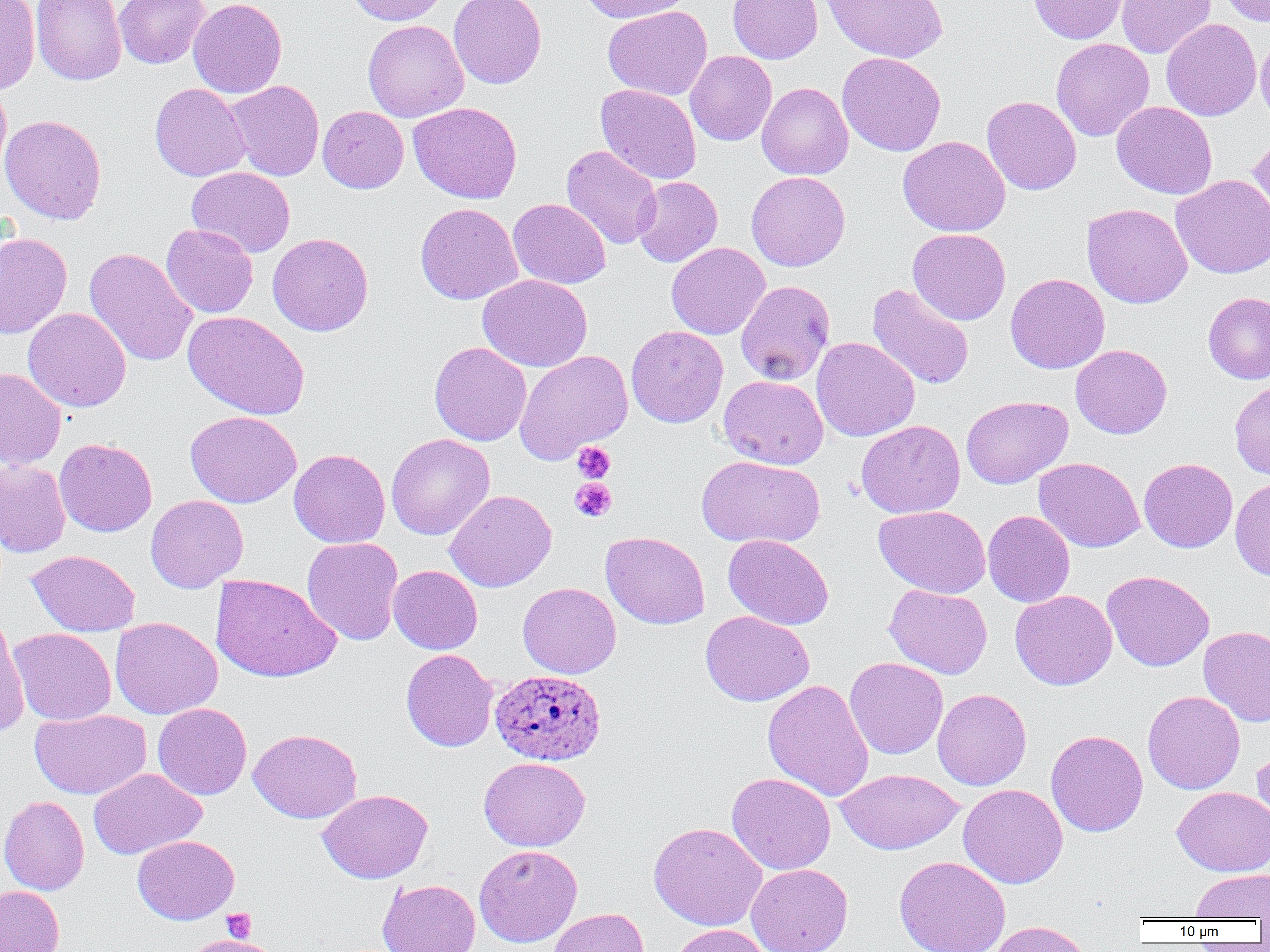
slide-level diagnosis = Plasmodium ovale
magnification = 1000x
image size = 1270×952 pixels
field of view = single
Plasmodium ovale-infected red blood cell locations = approximate bounding boxes as named x1/y1/x2/y2 corners in pixels: (x1=487, y1=668, x2=603, y2=764)
uninfected red blood cell locations = approximate bounding boxes as named x1/y1/x2/y2 corners in pixels: (x1=0, y1=0, x2=40, y2=95), (x1=31, y1=0, x2=127, y2=86), (x1=114, y1=0, x2=211, y2=69), (x1=188, y1=0, x2=287, y2=98), (x1=347, y1=0, x2=448, y2=26), (x1=449, y1=0, x2=547, y2=89), (x1=577, y1=0, x2=693, y2=24), (x1=727, y1=0, x2=823, y2=63), (x1=822, y1=0, x2=948, y2=63), (x1=1027, y1=0, x2=1129, y2=44), (x1=1116, y1=0, x2=1215, y2=58), (x1=1218, y1=0, x2=1270, y2=27), (x1=602, y1=6, x2=713, y2=100), (x1=1161, y1=18, x2=1261, y2=121), (x1=362, y1=19, x2=469, y2=122), (x1=1255, y1=30, x2=1270, y2=129), (x1=1051, y1=37, x2=1154, y2=141), (x1=685, y1=50, x2=777, y2=146), (x1=837, y1=52, x2=946, y2=156), (x1=226, y1=80, x2=324, y2=180), (x1=0, y1=81, x2=12, y2=180), (x1=756, y1=82, x2=853, y2=180), (x1=150, y1=83, x2=250, y2=181), (x1=596, y1=83, x2=702, y2=184), (x1=981, y1=95, x2=1081, y2=195), (x1=408, y1=101, x2=522, y2=204), (x1=1112, y1=101, x2=1217, y2=199), (x1=318, y1=105, x2=409, y2=193), (x1=0, y1=114, x2=107, y2=224), (x1=1248, y1=131, x2=1270, y2=226), (x1=898, y1=135, x2=1010, y2=237), (x1=561, y1=145, x2=662, y2=250), (x1=187, y1=166, x2=295, y2=258), (x1=745, y1=171, x2=850, y2=271), (x1=1170, y1=174, x2=1270, y2=278), (x1=633, y1=176, x2=723, y2=267), (x1=508, y1=198, x2=611, y2=289), (x1=415, y1=203, x2=523, y2=305), (x1=1082, y1=203, x2=1193, y2=308), (x1=161, y1=223, x2=258, y2=318), (x1=908, y1=228, x2=1010, y2=325), (x1=0, y1=232, x2=72, y2=339), (x1=267, y1=233, x2=373, y2=336), (x1=666, y1=242, x2=770, y2=340), (x1=84, y1=248, x2=198, y2=367), (x1=1005, y1=272, x2=1110, y2=374), (x1=478, y1=274, x2=592, y2=372), (x1=736, y1=281, x2=836, y2=385), (x1=867, y1=283, x2=974, y2=390), (x1=1203, y1=292, x2=1270, y2=384), (x1=22, y1=308, x2=131, y2=412), (x1=182, y1=311, x2=309, y2=420), (x1=626, y1=325, x2=728, y2=428), (x1=811, y1=337, x2=920, y2=442), (x1=429, y1=342, x2=531, y2=446), (x1=1071, y1=344, x2=1172, y2=439), (x1=515, y1=350, x2=633, y2=463), (x1=0, y1=368, x2=66, y2=469), (x1=719, y1=375, x2=828, y2=469), (x1=1229, y1=380, x2=1270, y2=481), (x1=961, y1=396, x2=1072, y2=489), (x1=185, y1=411, x2=301, y2=508), (x1=856, y1=420, x2=966, y2=518), (x1=386, y1=434, x2=495, y2=539), (x1=54, y1=438, x2=157, y2=537), (x1=289, y1=448, x2=391, y2=548), (x1=697, y1=455, x2=825, y2=548), (x1=1034, y1=457, x2=1144, y2=552), (x1=1139, y1=457, x2=1238, y2=553), (x1=0, y1=460, x2=71, y2=558), (x1=1230, y1=478, x2=1270, y2=581), (x1=445, y1=489, x2=556, y2=592), (x1=145, y1=495, x2=248, y2=593), (x1=874, y1=505, x2=991, y2=598), (x1=983, y1=510, x2=1075, y2=608), (x1=600, y1=531, x2=710, y2=629), (x1=723, y1=534, x2=834, y2=630), (x1=302, y1=537, x2=404, y2=645), (x1=26, y1=550, x2=140, y2=636), (x1=388, y1=565, x2=483, y2=654), (x1=1102, y1=570, x2=1214, y2=671), (x1=210, y1=574, x2=341, y2=683), (x1=518, y1=582, x2=621, y2=678), (x1=884, y1=584, x2=992, y2=679), (x1=1010, y1=589, x2=1117, y2=690), (x1=701, y1=611, x2=814, y2=706), (x1=0, y1=617, x2=30, y2=735), (x1=110, y1=617, x2=222, y2=719), (x1=1198, y1=626, x2=1270, y2=727), (x1=9, y1=628, x2=116, y2=726), (x1=400, y1=649, x2=498, y2=752), (x1=845, y1=657, x2=948, y2=759), (x1=763, y1=679, x2=874, y2=801), (x1=932, y1=688, x2=1032, y2=790), (x1=1143, y1=690, x2=1245, y2=794), (x1=153, y1=702, x2=252, y2=800), (x1=30, y1=709, x2=151, y2=800), (x1=248, y1=728, x2=362, y2=823), (x1=1046, y1=729, x2=1148, y2=836), (x1=1252, y1=742, x2=1270, y2=834), (x1=479, y1=756, x2=591, y2=852), (x1=88, y1=768, x2=206, y2=859), (x1=835, y1=768, x2=965, y2=855), (x1=726, y1=773, x2=836, y2=875), (x1=958, y1=784, x2=1068, y2=888), (x1=1172, y1=786, x2=1270, y2=876), (x1=318, y1=789, x2=433, y2=883), (x1=0, y1=795, x2=90, y2=895), (x1=648, y1=822, x2=767, y2=930), (x1=132, y1=835, x2=239, y2=925), (x1=473, y1=844, x2=583, y2=947), (x1=894, y1=855, x2=1010, y2=952), (x1=746, y1=863, x2=853, y2=952), (x1=1190, y1=869, x2=1270, y2=920), (x1=378, y1=878, x2=480, y2=952), (x1=0, y1=885, x2=64, y2=952), (x1=548, y1=907, x2=649, y2=952), (x1=985, y1=921, x2=1095, y2=952), (x1=668, y1=924, x2=775, y2=952), (x1=185, y1=934, x2=279, y2=952)
platelet locations = approximate bounding boxes as named x1/y1/x2/y2 corners in pixels: (x1=573, y1=442, x2=615, y2=482), (x1=570, y1=478, x2=617, y2=522), (x1=221, y1=907, x2=257, y2=943)
preparation = thin blood smear
modality = light microscopy